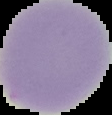
preparation: thin blood film
image_type: cell region segmented out of the field of view; surrounding area masked to black
result: no malaria parasites detected
image_size: 112×115 pixels